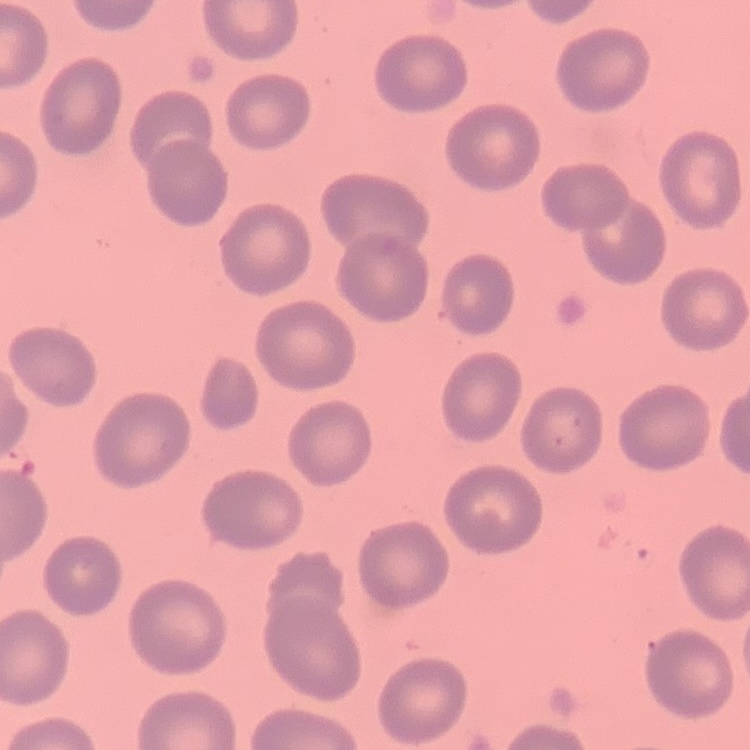

red_blood_cell_morphology: no rouleaux formation
stain: Field's or Giemsa
preparation: thin blood smear
image_type: one tile cut from a larger photomicrograph